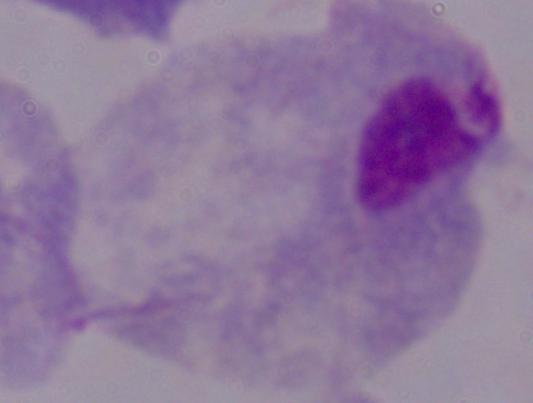 Micrograph. A trichomonad is shown. 1000x magnification.